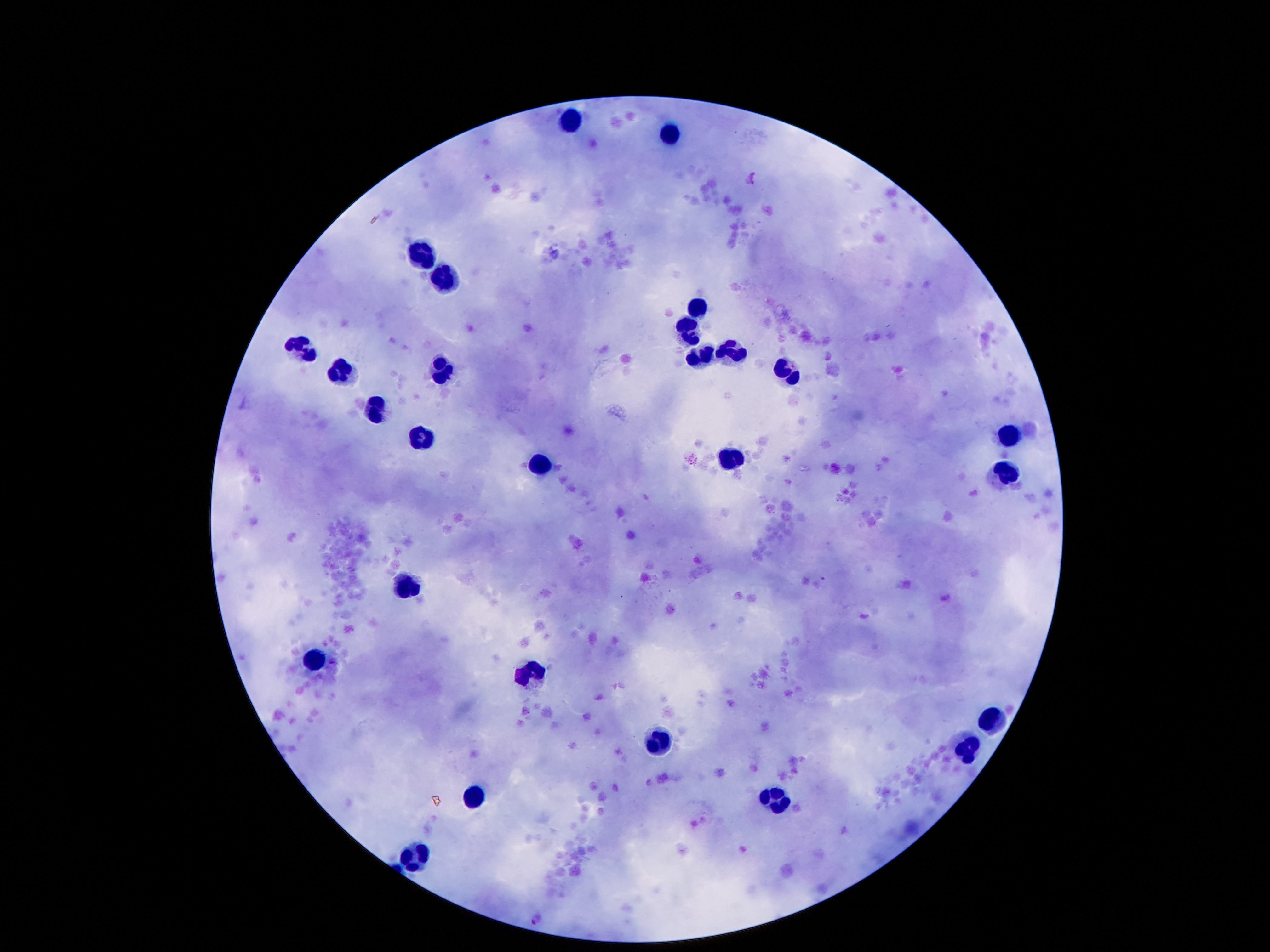

field of view = single
magnification = 100x
leukocyte locations = approximate centers as (x, y) in pixels: (569, 121), (669, 136), (423, 251), (444, 272), (700, 310), (689, 327), (303, 349), (734, 352), (703, 358), (442, 370), (339, 371), (790, 373), (374, 412), (1010, 436), (423, 438), (734, 460), (537, 469), (1003, 476), (410, 585), (317, 659), (532, 673), (991, 719), (662, 740), (969, 750), (475, 793), (780, 800), (417, 855)
patient malaria status = negative
capture = smartphone camera through the microscope eyepiece
image size = 1270×952 pixels
stain = Giemsa
preparation = thick peripheral-blood smear